Locate and identify every blood parasite.
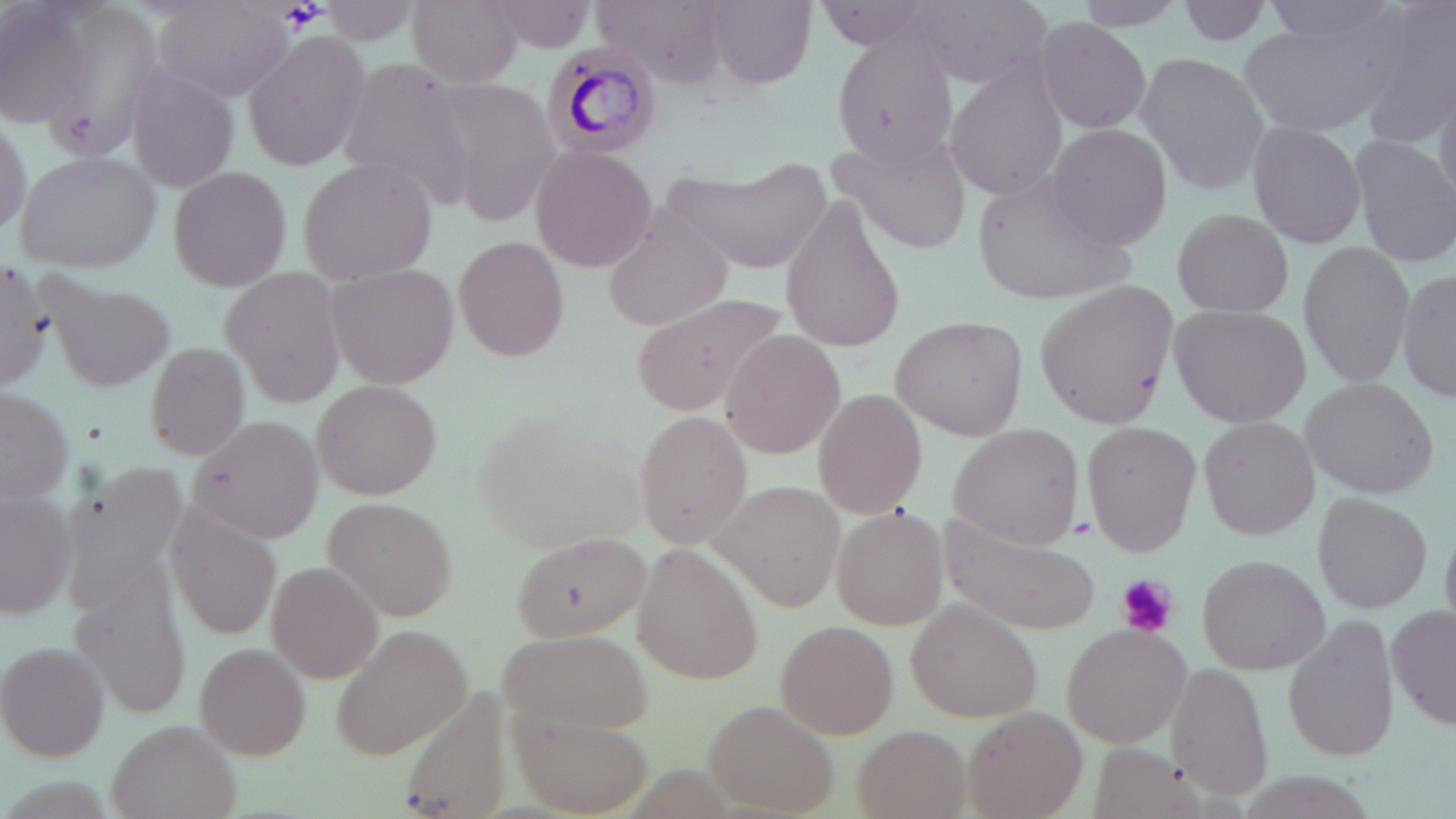
Approximate bounding boxes as named x1/y1/x2/y2 corners in pixels.
Plasmodium malariae-infected red blood cells: (x1=544, y1=40, x2=662, y2=162).
No Plasmodium falciparum, Plasmodium ovale, Plasmodium vivax, Babesia divergens, or Trypanosoma brucei observed.

slide-level diagnosis = Plasmodium malariae
modality = optical microscopy
stain = May-Grünwald-Giemsa
platelet locations = approximate bounding boxes as named x1/y1/x2/y2 corners in pixels: (x1=1113, y1=574, x2=1179, y2=637)
image size = 1456×819 pixels
uninfected red blood cell locations = approximate bounding boxes as named x1/y1/x2/y2 corners in pixels: (x1=2, y1=0, x2=91, y2=125), (x1=1255, y1=0, x2=1412, y2=53), (x1=1355, y1=0, x2=1456, y2=148), (x1=155, y1=1, x2=298, y2=101), (x1=320, y1=1, x2=424, y2=49), (x1=407, y1=1, x2=523, y2=88), (x1=484, y1=1, x2=600, y2=56), (x1=701, y1=1, x2=816, y2=90), (x1=902, y1=1, x2=1050, y2=88), (x1=1068, y1=1, x2=1187, y2=31), (x1=1178, y1=1, x2=1276, y2=50), (x1=595, y1=2, x2=731, y2=89), (x1=1240, y1=14, x2=1402, y2=136), (x1=1028, y1=17, x2=1153, y2=132), (x1=827, y1=24, x2=959, y2=170), (x1=243, y1=28, x2=373, y2=172), (x1=1133, y1=52, x2=1271, y2=196), (x1=334, y1=55, x2=472, y2=200), (x1=944, y1=58, x2=1070, y2=200), (x1=124, y1=67, x2=241, y2=192), (x1=430, y1=77, x2=558, y2=221), (x1=1433, y1=82, x2=1456, y2=206), (x1=0, y1=108, x2=32, y2=245), (x1=1245, y1=120, x2=1367, y2=250), (x1=1044, y1=123, x2=1173, y2=250), (x1=824, y1=130, x2=971, y2=254), (x1=1347, y1=134, x2=1454, y2=266), (x1=529, y1=142, x2=656, y2=273), (x1=15, y1=149, x2=161, y2=274), (x1=297, y1=155, x2=440, y2=285), (x1=659, y1=155, x2=833, y2=276), (x1=167, y1=167, x2=293, y2=292), (x1=971, y1=167, x2=1139, y2=308), (x1=779, y1=192, x2=908, y2=352), (x1=601, y1=208, x2=733, y2=331), (x1=1168, y1=208, x2=1296, y2=319), (x1=454, y1=233, x2=572, y2=364), (x1=1297, y1=242, x2=1416, y2=389), (x1=0, y1=259, x2=53, y2=389), (x1=326, y1=261, x2=461, y2=390), (x1=220, y1=266, x2=347, y2=406), (x1=1397, y1=266, x2=1456, y2=403), (x1=42, y1=272, x2=176, y2=393), (x1=1037, y1=280, x2=1177, y2=428), (x1=628, y1=292, x2=793, y2=415), (x1=1167, y1=303, x2=1311, y2=427), (x1=890, y1=317, x2=1026, y2=439), (x1=718, y1=329, x2=844, y2=461), (x1=141, y1=341, x2=254, y2=462), (x1=1300, y1=375, x2=1439, y2=499), (x1=310, y1=378, x2=442, y2=500), (x1=0, y1=380, x2=74, y2=507), (x1=811, y1=389, x2=927, y2=519), (x1=469, y1=405, x2=642, y2=552), (x1=634, y1=412, x2=754, y2=552), (x1=188, y1=414, x2=327, y2=544), (x1=1199, y1=414, x2=1319, y2=540), (x1=1080, y1=421, x2=1201, y2=553), (x1=947, y1=424, x2=1087, y2=549), (x1=57, y1=457, x2=191, y2=616), (x1=714, y1=479, x2=848, y2=614), (x1=0, y1=487, x2=78, y2=620), (x1=1311, y1=492, x2=1432, y2=615), (x1=322, y1=496, x2=457, y2=621), (x1=163, y1=503, x2=283, y2=644), (x1=828, y1=503, x2=950, y2=631), (x1=938, y1=513, x2=1103, y2=637), (x1=509, y1=530, x2=649, y2=646), (x1=634, y1=543, x2=765, y2=684), (x1=1196, y1=553, x2=1329, y2=676), (x1=267, y1=561, x2=382, y2=683), (x1=69, y1=564, x2=196, y2=720), (x1=905, y1=596, x2=1044, y2=724), (x1=1387, y1=602, x2=1456, y2=732), (x1=1282, y1=611, x2=1400, y2=764), (x1=774, y1=619, x2=900, y2=739), (x1=331, y1=621, x2=472, y2=762), (x1=1061, y1=623, x2=1192, y2=747), (x1=497, y1=624, x2=654, y2=735), (x1=1, y1=642, x2=111, y2=760), (x1=195, y1=642, x2=311, y2=757), (x1=1165, y1=662, x2=1273, y2=802), (x1=704, y1=700, x2=841, y2=816), (x1=508, y1=707, x2=654, y2=816), (x1=965, y1=708, x2=1088, y2=819), (x1=105, y1=718, x2=242, y2=819), (x1=851, y1=728, x2=974, y2=817), (x1=1085, y1=742, x2=1213, y2=819)
field of view = one of a larger specimen
preparation = thin blood smear
magnification = 1000x